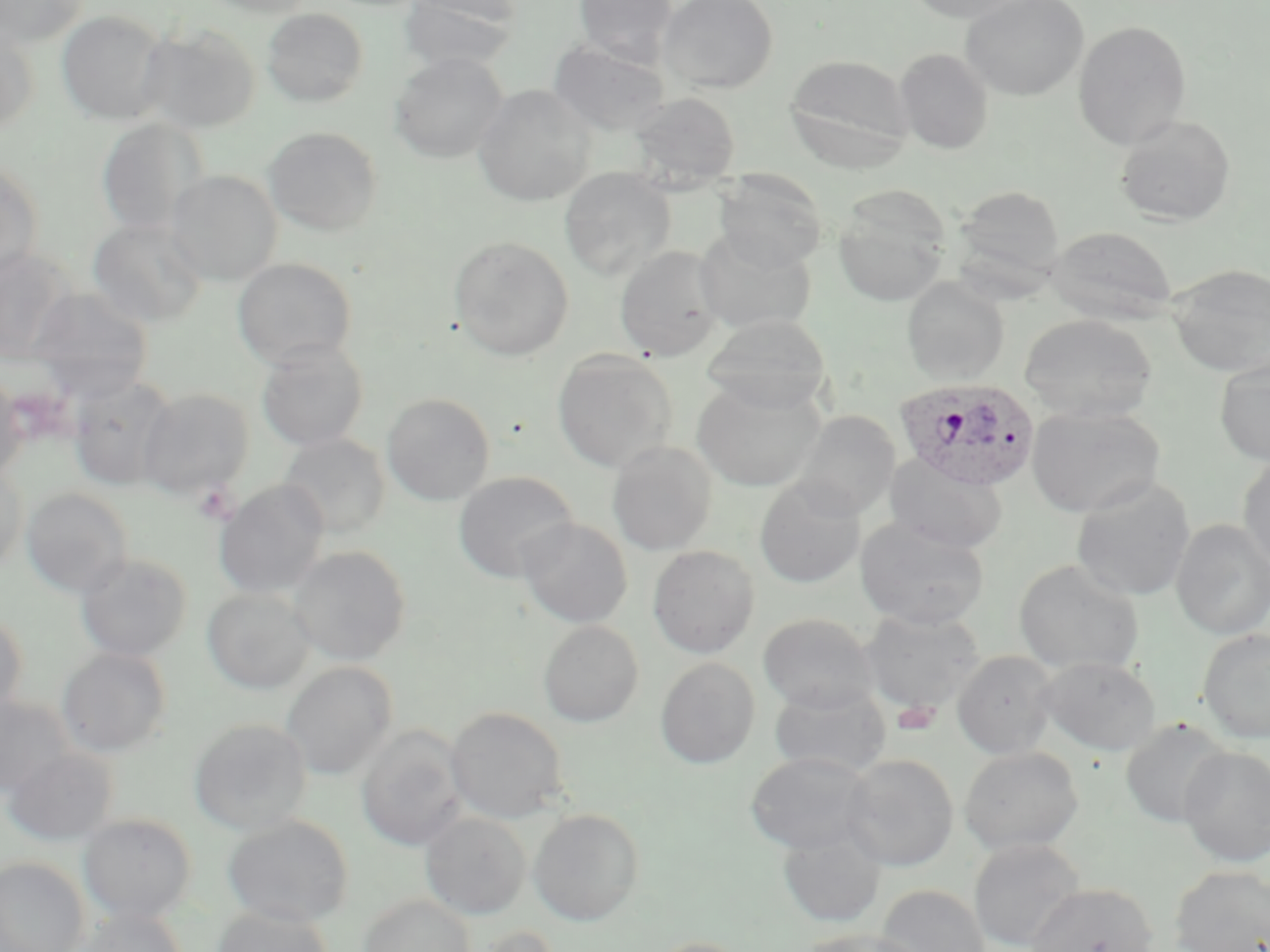
{
  "slide_level_diagnosis": "Plasmodium ovale",
  "uninfected_red_blood_cell_locations": "approximate bounding boxes as (x1, y1, x2, y2) in pixels: (0, 0, 90, 48), (198, 0, 319, 17), (399, 0, 520, 73), (573, 0, 677, 65), (657, 0, 779, 93), (903, 0, 1038, 24), (960, 0, 1089, 101), (262, 8, 368, 107), (56, 10, 171, 125), (1072, 20, 1192, 149), (0, 24, 39, 134), (138, 24, 261, 133), (548, 40, 670, 136), (894, 48, 993, 154), (390, 52, 507, 163), (784, 53, 915, 169), (473, 84, 596, 206), (628, 91, 741, 183), (1114, 115, 1236, 226), (97, 117, 207, 237), (263, 126, 383, 236), (0, 159, 44, 280), (559, 167, 676, 281), (164, 169, 283, 286), (714, 172, 827, 271), (952, 184, 1066, 294), (833, 191, 951, 308), (87, 218, 208, 327), (1047, 226, 1178, 323), (694, 228, 817, 334), (448, 235, 574, 360), (614, 245, 724, 361), (0, 248, 76, 362), (232, 257, 357, 368), (1167, 263, 1270, 377), (902, 277, 1009, 385), (26, 286, 153, 401), (701, 314, 831, 412), (1019, 314, 1157, 424), (255, 340, 370, 451), (552, 350, 678, 473), (1214, 354, 1270, 465), (0, 375, 26, 481), (67, 375, 179, 491), (692, 378, 826, 492), (137, 387, 255, 500), (382, 392, 495, 505), (1026, 405, 1165, 518), (794, 411, 900, 520), (278, 433, 391, 539), (607, 441, 717, 555), (884, 453, 1007, 554), (1237, 454, 1270, 573), (0, 466, 27, 575), (453, 471, 578, 582), (1071, 477, 1196, 601), (754, 478, 865, 588), (214, 480, 328, 599), (22, 487, 133, 598), (517, 518, 633, 628), (855, 518, 990, 629), (1171, 520, 1270, 639), (289, 545, 411, 665), (647, 545, 759, 658), (75, 552, 193, 662), (1014, 559, 1144, 674), (202, 587, 315, 693), (860, 608, 986, 713), (0, 610, 27, 721), (758, 612, 878, 712), (538, 620, 644, 727), (1197, 628, 1270, 743), (57, 646, 172, 757), (953, 650, 1058, 758), (1038, 656, 1161, 754), (655, 657, 760, 768), (282, 661, 397, 780), (769, 683, 892, 778), (0, 695, 79, 797), (446, 707, 568, 823), (1120, 717, 1232, 829), (189, 718, 311, 836), (357, 726, 467, 852), (1, 746, 118, 846), (959, 746, 1083, 856), (1178, 746, 1270, 867), (746, 751, 878, 855), (842, 753, 959, 871), (529, 808, 645, 925), (420, 811, 531, 919), (78, 813, 196, 922), (223, 815, 354, 927), (776, 822, 887, 929), (968, 837, 1086, 952), (0, 857, 88, 952), (1170, 864, 1270, 952), (1025, 882, 1158, 952), (876, 884, 990, 952), (359, 893, 475, 952), (211, 905, 333, 952), (74, 907, 187, 952), (472, 924, 563, 952), (801, 928, 929, 952), (644, 936, 750, 952)",
  "modality": "optical microscopy",
  "image_size": "1270×952 pixels",
  "plasmodium_ovale_infected_red_blood_cell_locations": "approximate bounding boxes as (x1, y1, x2, y2) in pixels: (896, 377, 1041, 492)",
  "preparation": "thin blood smear",
  "stain": "May-Grünwald-Giemsa",
  "platelet_locations": "approximate bounding boxes as (x1, y1, x2, y2) in pixels: (194, 484, 237, 523), (894, 700, 939, 735)",
  "field_of_view": "single",
  "magnification": "1000x"
}